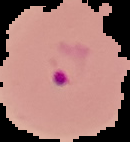 From a thin blood smear. Segmented cell region on a black background. Result: malaria parasites identified. Image is 130×142 pixels.